Locate every malaria parasite by life-cycle stage, and every leukocyte.
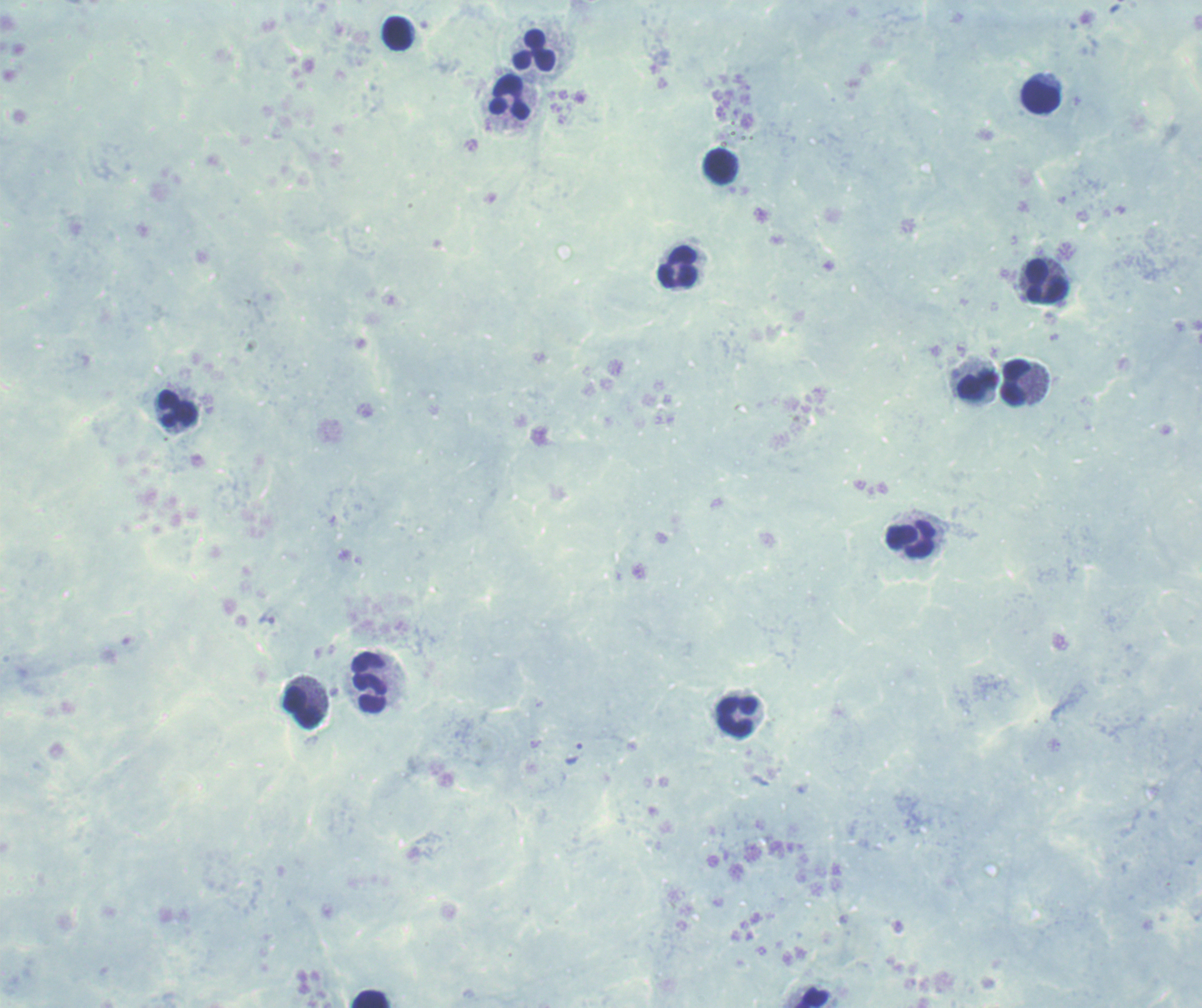
No malaria parasites seen.
Approximate centers as {x, y} in pixels.
Leukocytes: {397, 33}, {534, 51}, {508, 98}, {1041, 98}, {720, 167}, {678, 268}, {1046, 281}, {1015, 382}, {977, 386}, {177, 410}, {911, 540}, {369, 684}, {303, 708}, {736, 718}, {815, 998}, {371, 999}.

Summary:
  - Preparation: thick blood film
  - Background quality: poor
  - Context: previously used in an actual diagnosis
  - Magnification: 100x
  - Image size: 1202×1008 pixels
  - Stain: Romanowsky
  - Field of view: single